Give the extent of all Plasmodium falciparum-infected red blood cells.
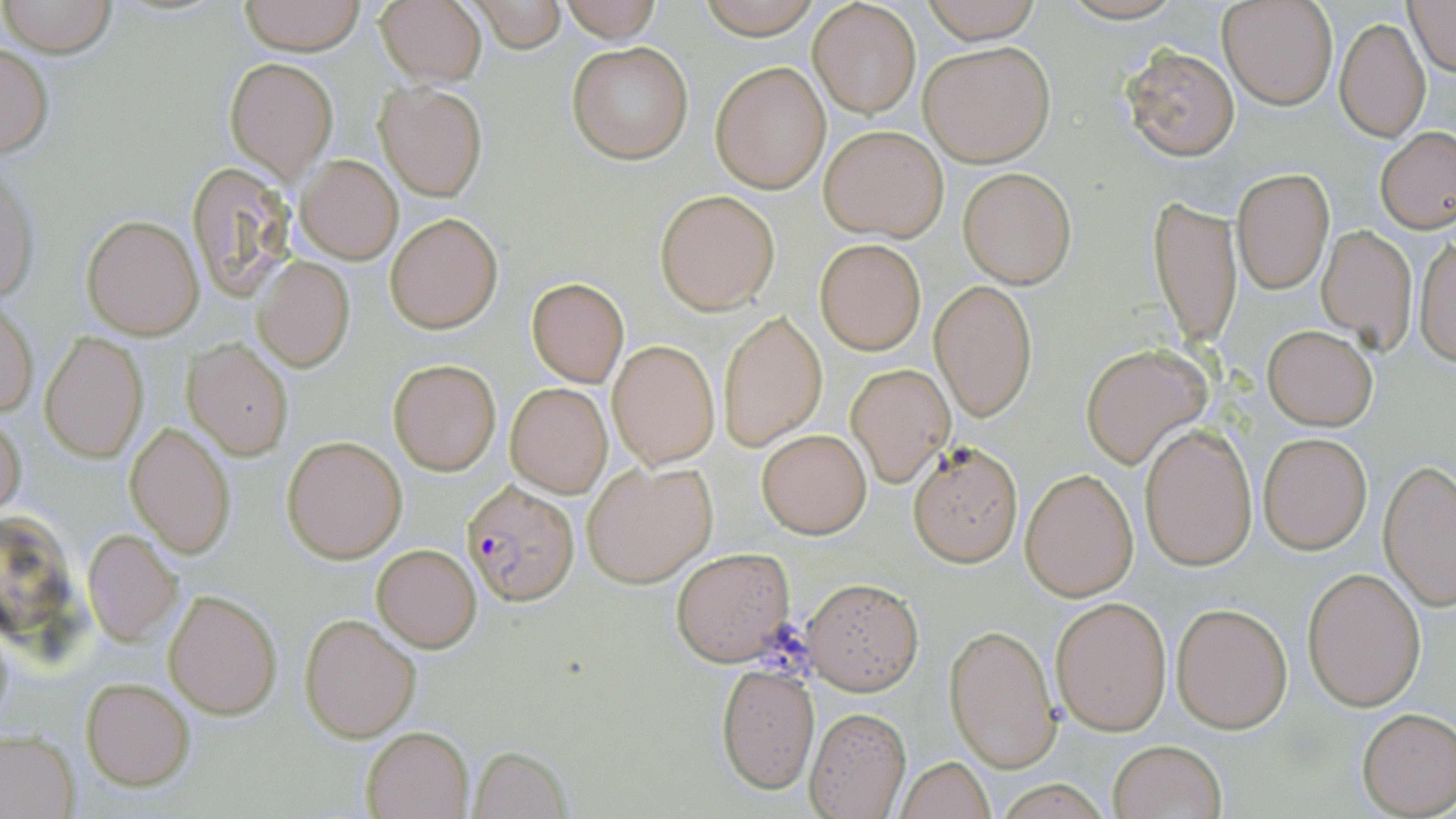
Approximate bounding boxes as named x1/y1/x2/y2 corners in pixels.
Plasmodium falciparum-infected red blood cells: (x1=462, y1=478, x2=580, y2=608).

Uninfected red blood cell locations: (x1=0, y1=0, x2=116, y2=57), (x1=238, y1=0, x2=365, y2=54), (x1=373, y1=0, x2=488, y2=88), (x1=468, y1=0, x2=569, y2=53), (x1=693, y1=0, x2=823, y2=36), (x1=920, y1=0, x2=1042, y2=43), (x1=1219, y1=0, x2=1338, y2=110), (x1=1405, y1=0, x2=1455, y2=76), (x1=556, y1=1, x2=665, y2=42), (x1=809, y1=2, x2=920, y2=119), (x1=1335, y1=17, x2=1430, y2=142), (x1=919, y1=40, x2=1055, y2=166), (x1=566, y1=41, x2=694, y2=165), (x1=0, y1=44, x2=54, y2=160), (x1=1123, y1=45, x2=1240, y2=161), (x1=226, y1=57, x2=338, y2=179), (x1=710, y1=60, x2=832, y2=194), (x1=374, y1=81, x2=487, y2=201), (x1=819, y1=125, x2=948, y2=241), (x1=1376, y1=127, x2=1456, y2=234), (x1=296, y1=155, x2=402, y2=264), (x1=184, y1=163, x2=298, y2=301), (x1=1233, y1=167, x2=1333, y2=293), (x1=0, y1=168, x2=39, y2=308), (x1=959, y1=168, x2=1077, y2=288), (x1=655, y1=189, x2=782, y2=314), (x1=1149, y1=195, x2=1242, y2=351), (x1=384, y1=212, x2=503, y2=334), (x1=81, y1=214, x2=203, y2=339), (x1=1316, y1=225, x2=1418, y2=350), (x1=1412, y1=232, x2=1456, y2=368), (x1=814, y1=239, x2=926, y2=354), (x1=253, y1=257, x2=355, y2=373), (x1=525, y1=277, x2=630, y2=388), (x1=930, y1=280, x2=1038, y2=422), (x1=1, y1=299, x2=38, y2=419), (x1=718, y1=311, x2=827, y2=450), (x1=1262, y1=324, x2=1378, y2=430), (x1=41, y1=332, x2=150, y2=464), (x1=184, y1=339, x2=294, y2=459), (x1=608, y1=339, x2=719, y2=468), (x1=1080, y1=347, x2=1207, y2=467), (x1=387, y1=358, x2=502, y2=476), (x1=845, y1=363, x2=954, y2=488), (x1=505, y1=382, x2=612, y2=498), (x1=0, y1=414, x2=26, y2=519), (x1=125, y1=421, x2=237, y2=560), (x1=1139, y1=426, x2=1258, y2=571), (x1=758, y1=429, x2=871, y2=538), (x1=1258, y1=432, x2=1372, y2=554), (x1=282, y1=436, x2=406, y2=563), (x1=906, y1=440, x2=1024, y2=566), (x1=1379, y1=459, x2=1456, y2=609), (x1=582, y1=460, x2=716, y2=588), (x1=1021, y1=469, x2=1139, y2=600), (x1=83, y1=530, x2=182, y2=649), (x1=371, y1=544, x2=482, y2=652), (x1=670, y1=547, x2=796, y2=666), (x1=1302, y1=566, x2=1426, y2=709), (x1=801, y1=576, x2=925, y2=694), (x1=164, y1=589, x2=282, y2=720), (x1=1050, y1=596, x2=1172, y2=735), (x1=1171, y1=601, x2=1293, y2=733), (x1=299, y1=614, x2=421, y2=742), (x1=944, y1=623, x2=1061, y2=772), (x1=716, y1=661, x2=820, y2=793), (x1=82, y1=678, x2=195, y2=790), (x1=805, y1=708, x2=911, y2=819), (x1=1357, y1=708, x2=1455, y2=816), (x1=361, y1=727, x2=474, y2=818), (x1=0, y1=729, x2=78, y2=819), (x1=1108, y1=739, x2=1227, y2=819), (x1=469, y1=746, x2=572, y2=818), (x1=897, y1=757, x2=996, y2=818). Slide-level diagnosis: Plasmodium falciparum. Image is 1456×819 pixels. Light microscopy. Thin blood smear. Single field of view. May-Grünwald-Giemsa-stained preparation. Captured at 1000x magnification.